Comment on the morphology of the erythrocytes.
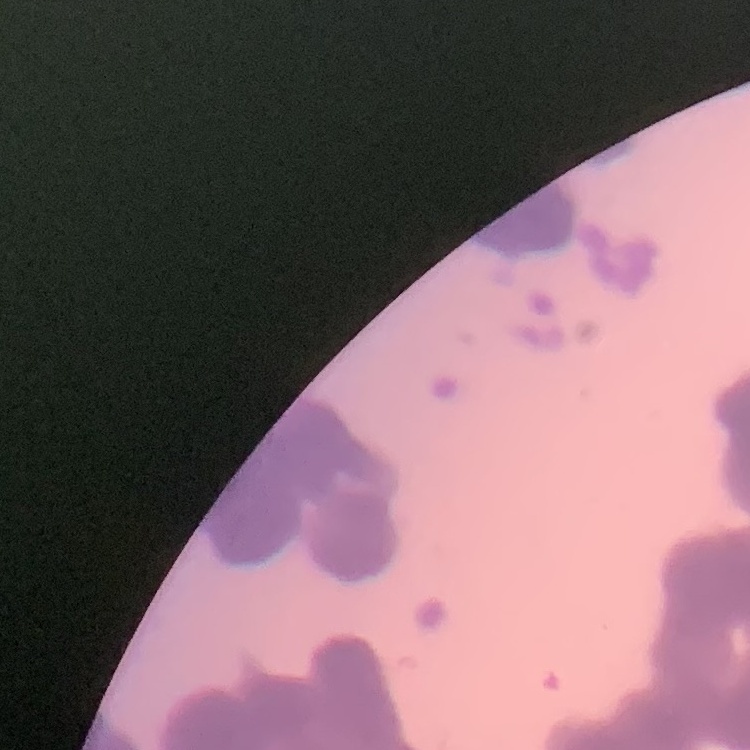

They show rouleaux formation.

Summary:
  - Preparation: thin blood film
  - Stain: Field's or Giemsa
  - Image type: one tile cut from a larger photomicrograph